Classify this cell by malaria status.
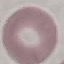

It is uninfected.

Summary:
  - Stain: Giemsa
  - Capture: smartphone camera at the microscope eyepiece
  - Image type: automatically extracted cell patch, resized to 64 × 64 pixels
  - Preparation: thin blood smear